Name the blood parasite species.
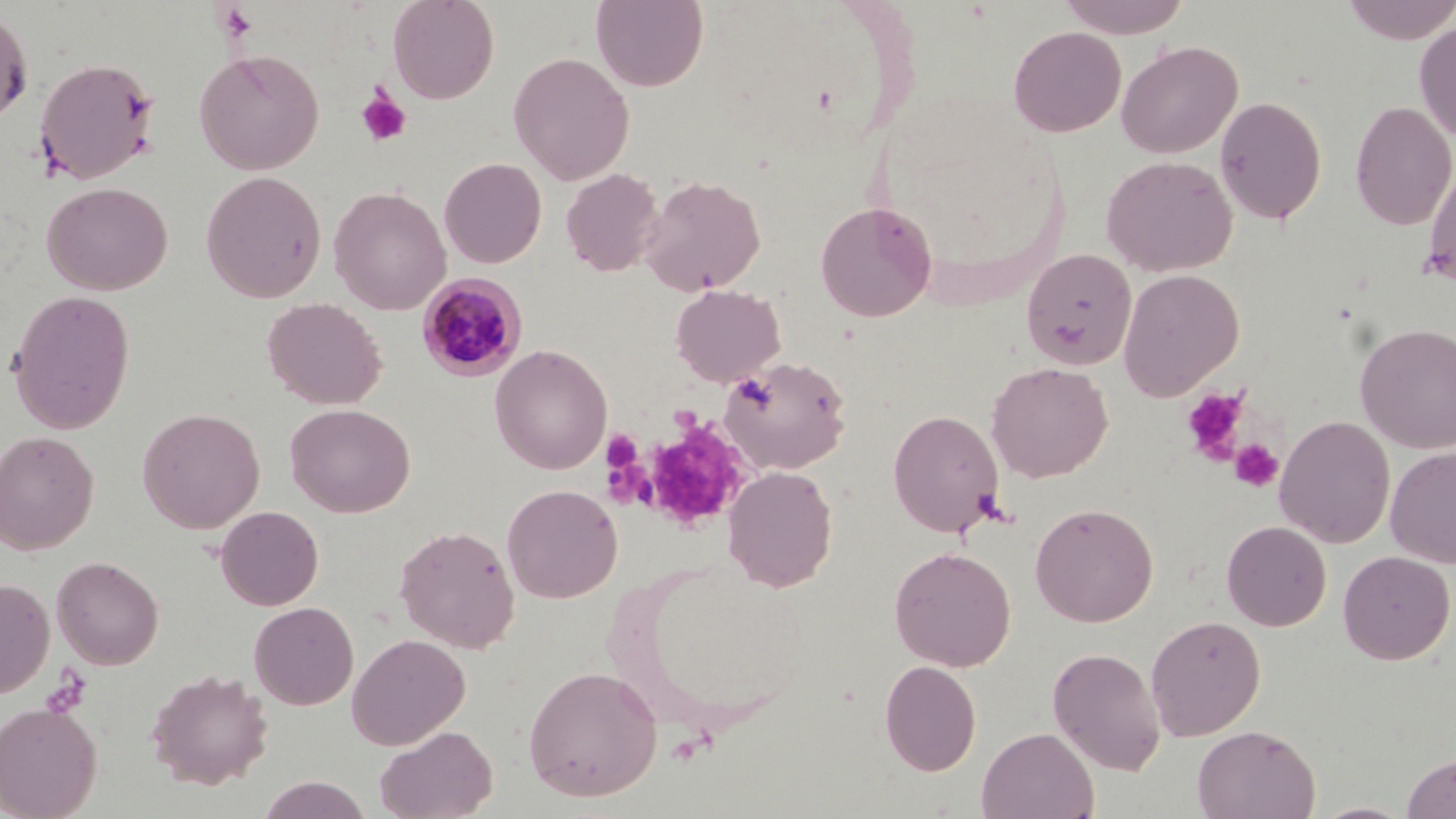

Plasmodium malariae.

{
  "uninfected_red_blood_cell_locations": "approximate bounding boxes as [x1, y1, x2, y2] in pixels: [387, 0, 499, 104], [591, 0, 708, 91], [1056, 0, 1192, 38], [1340, 0, 1456, 44], [0, 6, 34, 127], [1415, 19, 1456, 142], [1008, 25, 1126, 137], [1116, 41, 1243, 159], [193, 49, 324, 174], [508, 51, 635, 185], [34, 57, 159, 184], [1215, 95, 1327, 225], [1351, 101, 1456, 230], [1101, 155, 1238, 276], [1423, 156, 1456, 294], [439, 157, 547, 268], [561, 167, 663, 277], [201, 171, 326, 302], [640, 175, 766, 296], [42, 181, 173, 295], [329, 186, 451, 315], [815, 202, 937, 322], [1021, 248, 1137, 370], [1118, 268, 1244, 400], [671, 284, 785, 387], [8, 289, 136, 434], [262, 297, 387, 410], [1355, 322, 1456, 454], [490, 344, 612, 474], [719, 356, 851, 474], [986, 362, 1112, 482], [284, 403, 415, 517], [137, 407, 265, 533], [887, 409, 1004, 538], [1274, 415, 1395, 548], [0, 430, 99, 555], [1385, 445, 1456, 568], [722, 465, 838, 592], [501, 483, 622, 603], [1030, 502, 1159, 627], [215, 505, 324, 611], [1221, 520, 1332, 631], [393, 524, 521, 653], [889, 546, 1016, 671], [1337, 550, 1455, 664], [51, 555, 164, 669], [0, 576, 55, 699], [249, 601, 359, 710], [1145, 615, 1266, 741], [347, 634, 471, 750], [1047, 647, 1166, 776], [879, 659, 982, 775], [523, 665, 663, 802], [146, 668, 273, 789], [0, 701, 103, 819], [1192, 724, 1320, 819], [375, 725, 498, 819], [977, 726, 1099, 819], [1401, 753, 1456, 818], [256, 775, 372, 819], [1309, 801, 1415, 819]",
  "image_size": "1456×819 pixels",
  "platelet_locations": "approximate bounding boxes as [x1, y1, x2, y2] in pixels: [356, 89, 412, 147], [1181, 387, 1248, 464], [626, 416, 753, 533], [603, 430, 642, 471], [1229, 438, 1284, 492]",
  "magnification": "1000x",
  "field_of_view": "one of a larger specimen",
  "preparation": "thin blood smear",
  "plasmodium_malariae_infected_red_blood_cell_locations": "approximate bounding boxes as [x1, y1, x2, y2] in pixels: [417, 273, 529, 380]",
  "modality": "optical microscopy",
  "stain": "May-Grünwald-Giemsa"
}